Identify the blood parasite species.
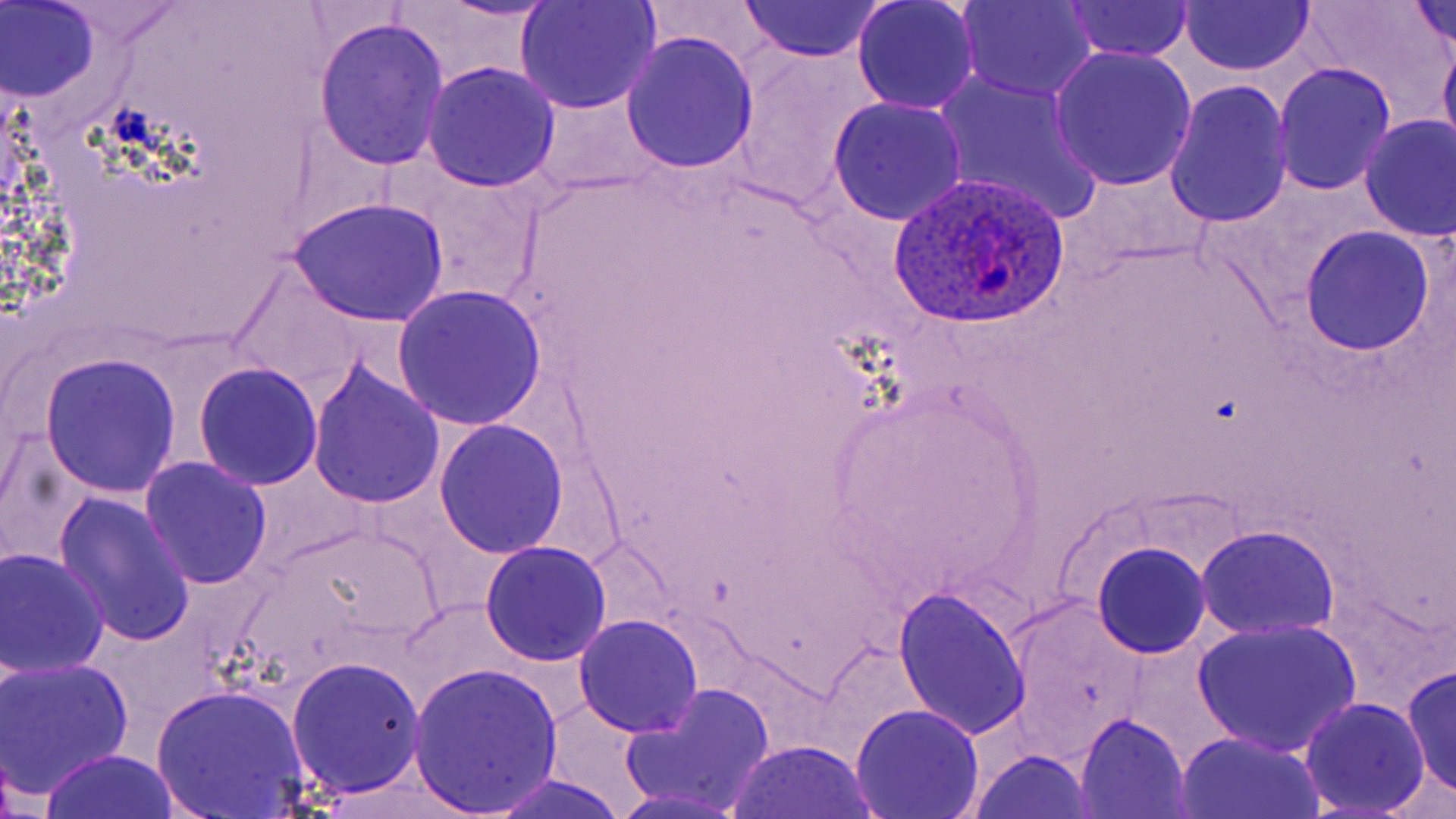
Plasmodium ovale.

magnification = 1000x
Plasmodium ovale-infected red blood cell locations = approximate bounding boxes as (x1, y1, x2, y2) in pixels: (888, 172, 1070, 327)
preparation = thin blood smear
uninfected red blood cell locations = approximate bounding boxes as (x1, y1, x2, y2) in pixels: (1, 0, 100, 103), (434, 0, 562, 23), (739, 0, 884, 63), (850, 0, 981, 115), (958, 0, 1099, 102), (1060, 0, 1194, 61), (1179, 0, 1316, 76), (1301, 0, 1445, 108), (1407, 0, 1456, 52), (515, 1, 663, 114), (313, 16, 451, 170), (620, 31, 759, 174), (1438, 33, 1456, 165), (1049, 45, 1196, 192), (726, 49, 877, 212), (421, 61, 561, 193), (1271, 62, 1397, 195), (933, 69, 1105, 227), (1162, 77, 1294, 227), (529, 92, 663, 195), (827, 96, 967, 226), (1357, 114, 1456, 243), (404, 171, 547, 303), (288, 195, 450, 327), (1299, 224, 1437, 356), (228, 265, 369, 399), (391, 283, 548, 432), (39, 352, 182, 497), (307, 359, 445, 509), (193, 362, 324, 489), (432, 419, 569, 558), (138, 455, 272, 592), (53, 489, 196, 647), (1196, 525, 1339, 639), (479, 541, 612, 665), (1091, 541, 1212, 658), (1, 548, 109, 679), (894, 585, 1031, 740), (1009, 600, 1148, 753), (574, 613, 705, 737), (1192, 618, 1360, 756), (0, 656, 133, 801), (286, 656, 426, 798), (1400, 663, 1455, 801), (407, 664, 563, 816), (620, 682, 777, 816), (151, 684, 311, 818), (1299, 696, 1432, 817), (849, 702, 985, 819), (1076, 711, 1194, 818), (1174, 729, 1322, 818), (727, 738, 878, 818), (38, 749, 181, 819), (970, 750, 1095, 819), (488, 773, 629, 818)
modality = optical microscopy
field of view = one of a larger specimen
image size = 1456×819 pixels
stain = May-Grünwald-Giemsa